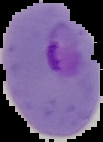

Image is 103×142 pixels. Cell region segmented out of the field of view; the surrounding area is masked to black. Malaria status: parasitized. From a thin blood smear.